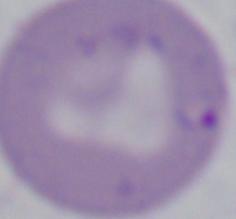
A Babesia parasite is shown. Photomicrograph. 1000x magnification.